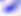

{
  "modality": "micrograph",
  "magnification": "400x",
  "identification": "Toxoplasma gondii"
}